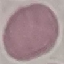
result = no malaria parasites detected
image type = automatically extracted cell patch, resized to 64 × 64 pixels
stain = Giemsa
preparation = thin blood smear
capture = smartphone camera at the microscope eyepiece